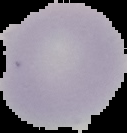
image_type: segmented cell region with the area outside set to black
result: no Plasmodium parasites seen
preparation: thin blood smear
image_size: 127×133 pixels